Give the position of every Plasmodium parasite visible.
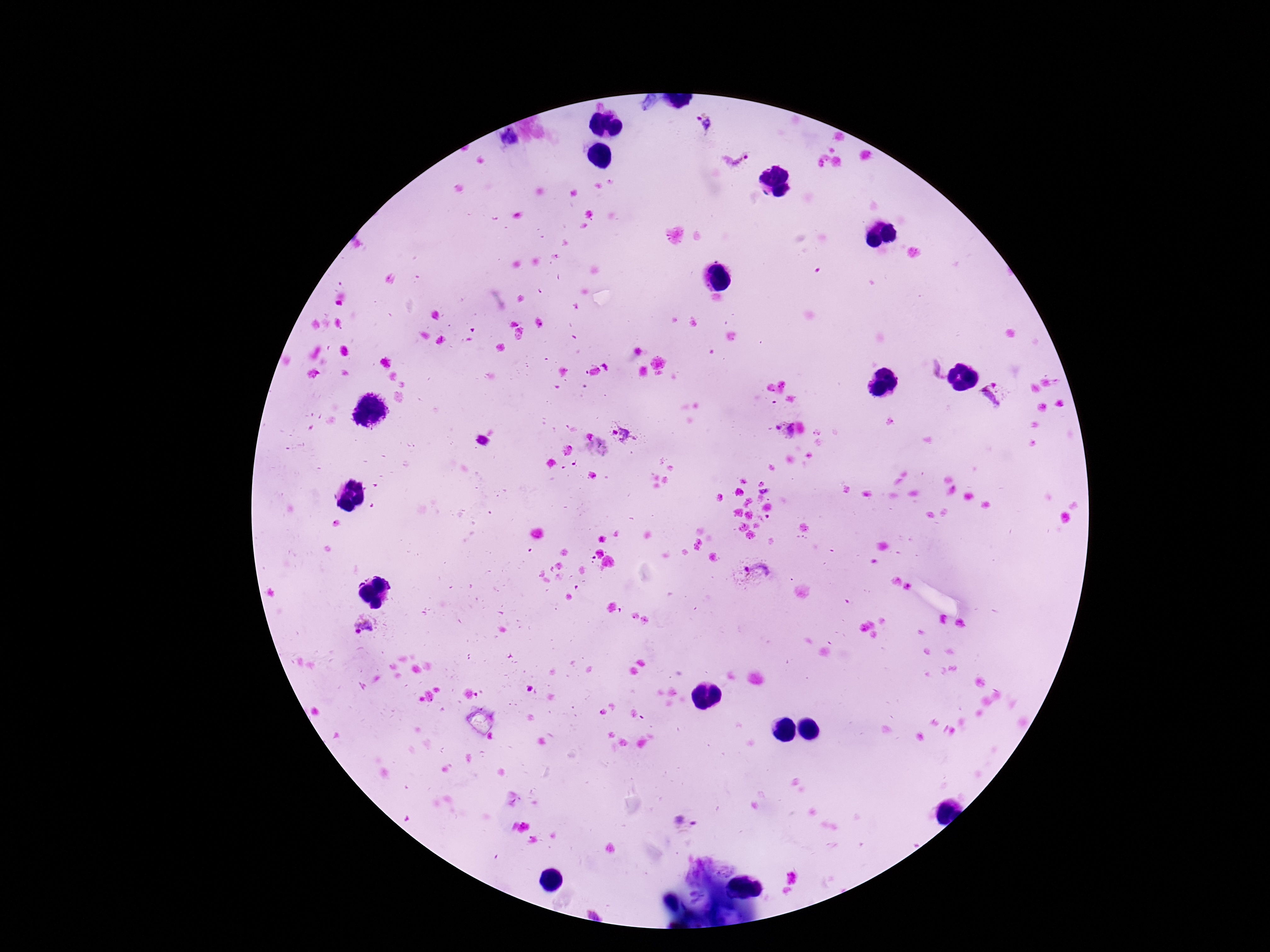

Approximate centers as {x, y} in pixels.
Plasmodium parasites: {703, 124}, {508, 138}, {737, 161}, {994, 395}, {784, 430}, {621, 433}, {755, 573}, {363, 626}, {686, 822}.

preparation = thick blood smear
image size = 1270×952 pixels
field of view = single
stain = Giemsa
magnification = 100x
capture = smartphone camera through the microscope eyepiece
patient malaria status = infected